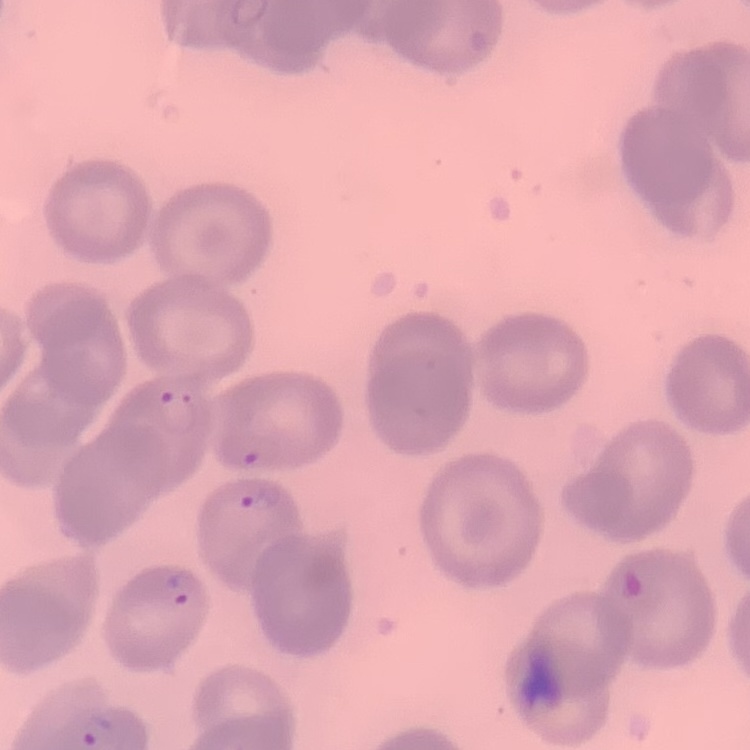

Summary:
  - Red blood cell morphology: no rouleaux formation
  - Stain: Field's or Giemsa
  - Image type: square crop of a larger photomicrograph
  - Preparation: thin blood film